Identify the parasite.
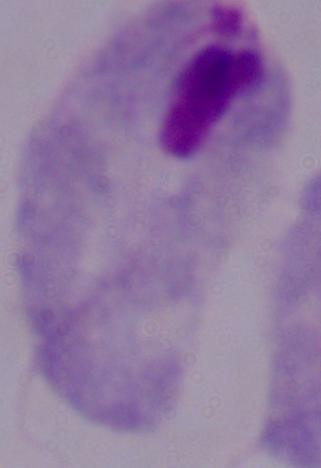

A trichomonad.

magnification = 1000x
modality = photomicrograph